State which cell type is depicted.
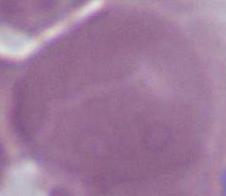
An erythrocyte.

magnification = 1000x
modality = photomicrograph